State which parasite is depicted.
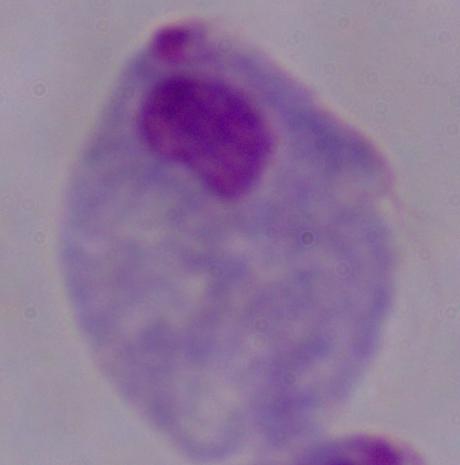

This is a trichomonad.

Summary:
  - Modality: micrograph
  - Magnification: 1000x